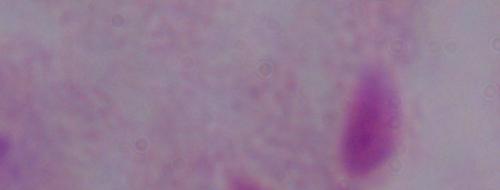

magnification = 1000x
modality = micrograph
identification = trichomonad